Name the parasite shown.
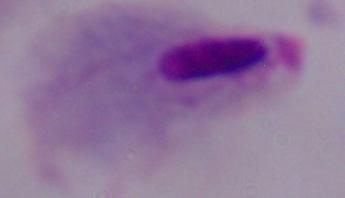

This is a trichomonad.

magnification = 1000x
modality = photomicrograph